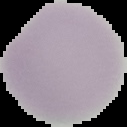
Segmented cell region on a black background. From a thin blood smear. Image is 127×127 pixels. Result: no Plasmodium parasites seen.